Classify this cell by malaria status.
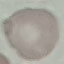

Uninfected.

Summary:
  - Image type: automatically extracted cell patch, resized to 64 × 64 pixels
  - Preparation: thin blood film
  - Stain: Giemsa
  - Capture: smartphone camera at the microscope eyepiece